Classify this cell by malaria status.
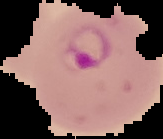
Parasitized.

image_size: 163×139 pixels
preparation: thin blood film
image_type: segmented cell region with the area outside set to black